Name the cell type shown.
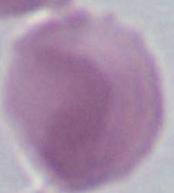
An erythrocyte.

1000x magnification. Micrograph.